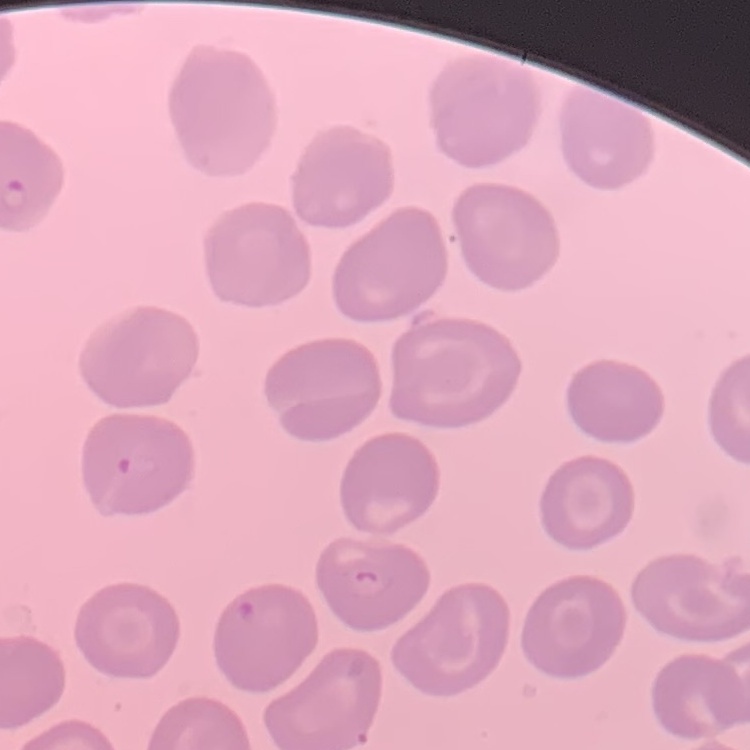
{
  "red_blood_cell_morphology": "no rouleaux formation",
  "image_type": "one tile cut from a larger photomicrograph",
  "stain": "Field's or Giemsa",
  "preparation": "thin peripheral smear"
}